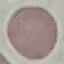

Summary:
  - Malaria status: uninfected
  - Image type: automatically extracted cell patch, resized to 64 × 64 pixels
  - Stain: Giemsa
  - Capture: smartphone through the microscope eyepiece
  - Preparation: thin blood film